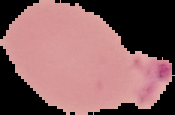 From a thin blood film. Malaria status: parasitized. Image is 175×115 pixels. Segmented cell region on a black background.